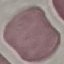
Malaria status: uninfected. Thin blood smear. Giemsa stain. Acquired by smartphone through the microscope eyepiece. Cell patch, automatically extracted from a larger field of view and resized to 64 × 64 pixels.